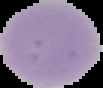

Image is 103×88 pixels. From a thin blood smear. The area outside the segmented cell region is set to black. Result: no Plasmodium parasites detected.